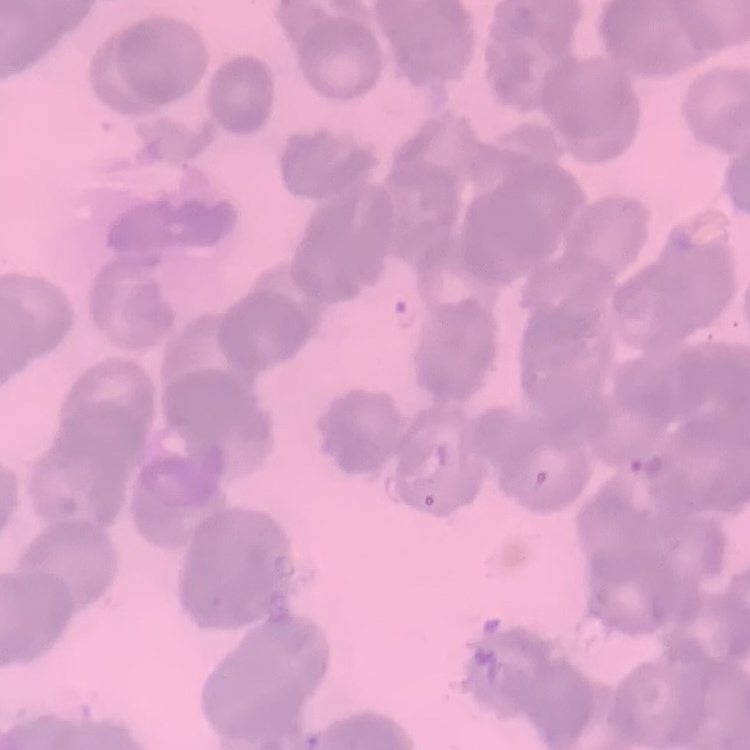

The erythrocytes show rouleaux formation. Thin peripheral smear. Field's or Giemsa stain. Square crop of a larger photomicrograph.